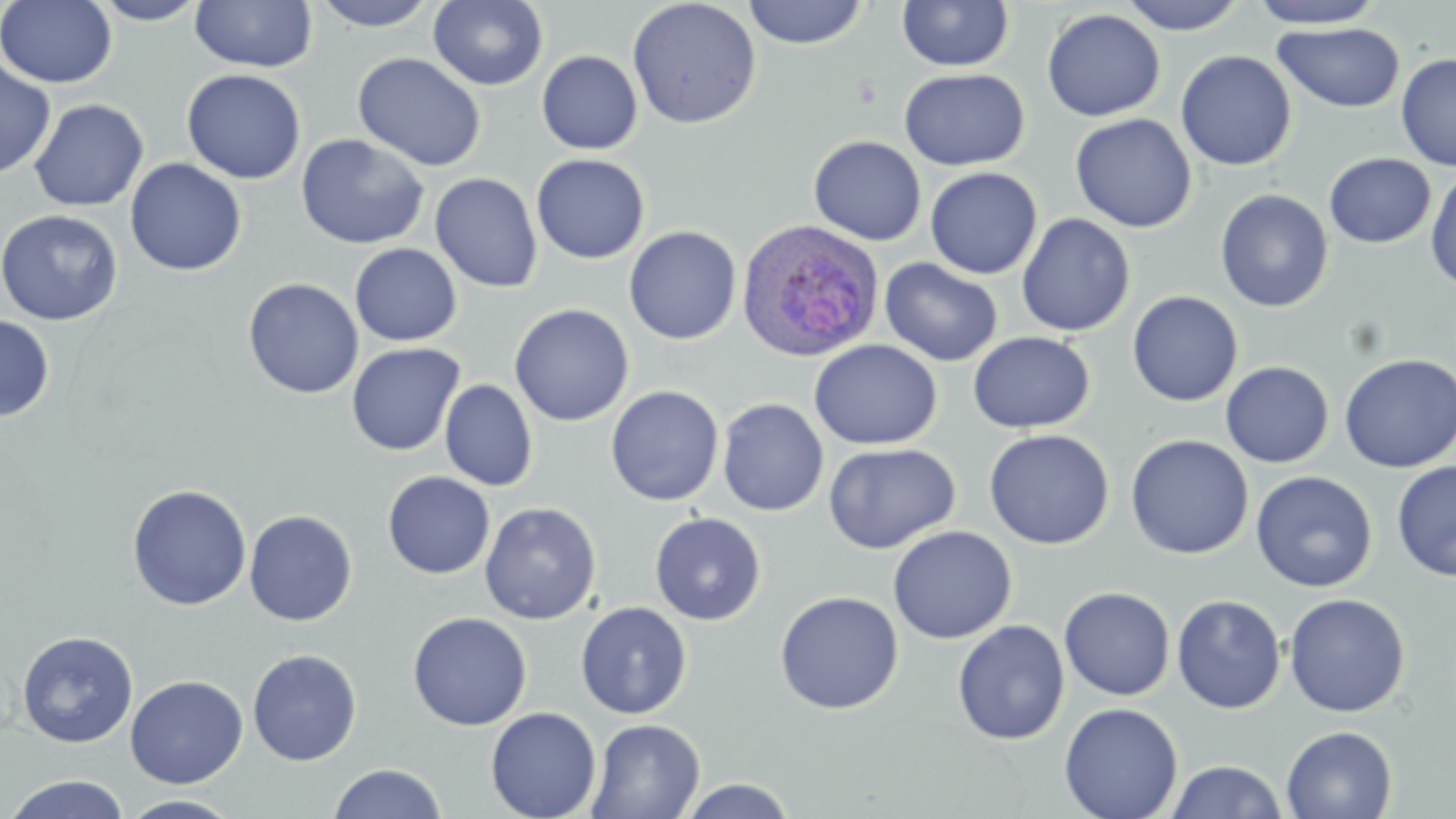

slide_level_diagnosis: Plasmodium ovale
magnification: 1000x
field_of_view: single
preparation: thin blood smear
uninfected_red_blood_cell_locations: 'approximate bounding boxes as (x1,y1)-(x2,y2) corner pairs in pixels: (1,0)-(117,88), (89,0)-(210,25), (190,0)-(317,72), (311,0)-(439,31), (428,0)-(548,91), (626,0)-(762,130), (741,0)-(869,49), (897,0)-(1015,71), (1117,0)-(1247,35), (1248,0)-(1385,28), (1042,9)-(1165,121), (1273,21)-(1405,113), (536,50)-(643,155), (1175,50)-(1296,171), (352,52)-(486,172), (1395,53)-(1456,172), (0,59)-(56,179), (181,68)-(306,184), (898,68)-(1029,170), (29,98)-(149,211), (1070,114)-(1197,233), (296,133)-(430,249), (808,135)-(926,246), (531,153)-(649,264), (1324,153)-(1436,248), (124,158)-(247,276), (925,166)-(1042,279), (1425,167)-(1456,292), (430,172)-(543,293), (1214,189)-(1333,313), (0,209)-(123,325), (1016,213)-(1136,337), (624,225)-(742,345), (350,243)-(462,346), (880,258)-(1003,367), (242,278)-(363,399), (1127,291)-(1243,407), (509,303)-(634,426), (0,315)-(55,423), (967,331)-(1095,434), (808,339)-(942,450), (346,343)-(465,456), (1339,352)-(1456,473), (1220,361)-(1334,468), (440,379)-(539,492), (605,385)-(724,506), (717,398)-(829,516), (984,428)-(1114,550), (1125,434)-(1254,559), (823,442)-(960,554), (1391,461)-(1456,581), (1251,470)-(1377,593), (382,471)-(495,579), (126,483)-(251,611), (479,501)-(602,624), (244,509)-(358,626), (650,512)-(766,626), (887,525)-(1017,644), (1059,586)-(1175,701), (774,590)-(904,715), (1284,593)-(1411,718), (1171,594)-(1286,714), (575,601)-(693,719), (407,611)-(532,731), (952,620)-(1069,745), (16,630)-(138,748), (247,648)-(363,766), (125,675)-(248,788), (1058,702)-(1183,819), (485,706)-(601,819), (586,718)-(705,819), (1281,725)-(1397,819), (1165,760)-(1288,818), (327,763)-(448,819), (4,774)-(131,818), (677,777)-(798,818), (120,794)-(243,818)'
image_size: 1456×819 pixels
stain: May-Grünwald-Giemsa
modality: optical microscopy
plasmodium_ovale_infected_red_blood_cell_locations: 'approximate bounding boxes as (x1,y1)-(x2,y2) corner pairs in pixels: (736,219)-(884,362)'